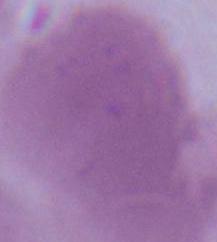

magnification = 1000x
identification = erythrocyte
modality = micrograph